Name the parasite shown.
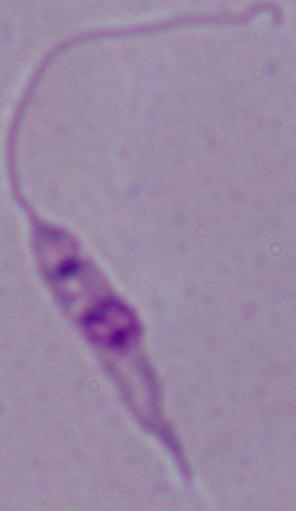
Leishmania.

Photomicrograph. 1000x magnification.